State which parasite is depicted.
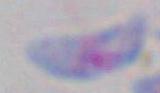

This is Toxoplasma gondii.

magnification = 1000x
modality = micrograph